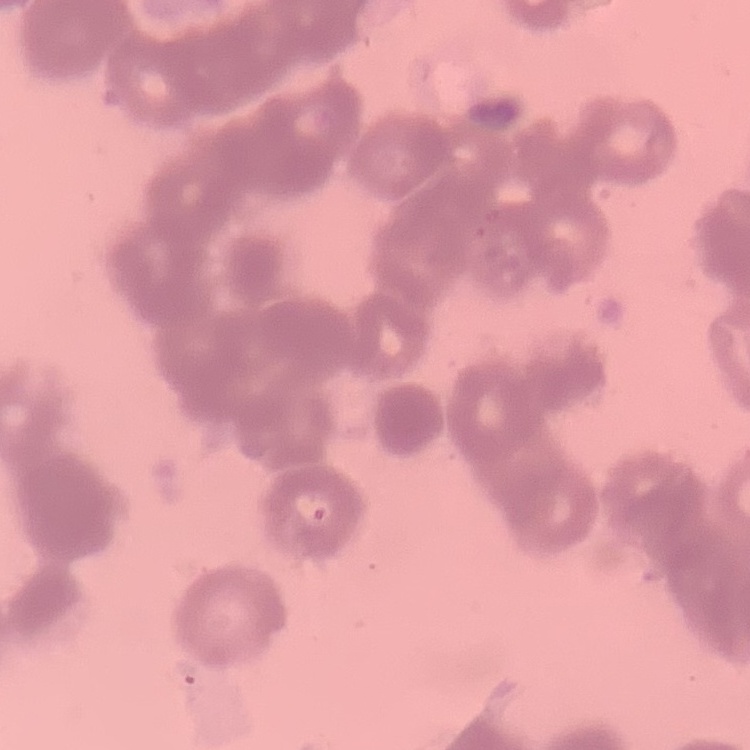
{
  "red_blood_cell_morphology": "rouleaux formation",
  "stain": "Field's or Giemsa",
  "image_type": "square crop of a larger photomicrograph",
  "preparation": "thin blood film"
}